Assess this cell for malaria.
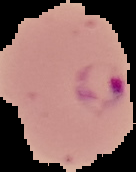
Parasitized.

preparation = thin blood film
image type = segmented cell region on a black background
image size = 136×172 pixels